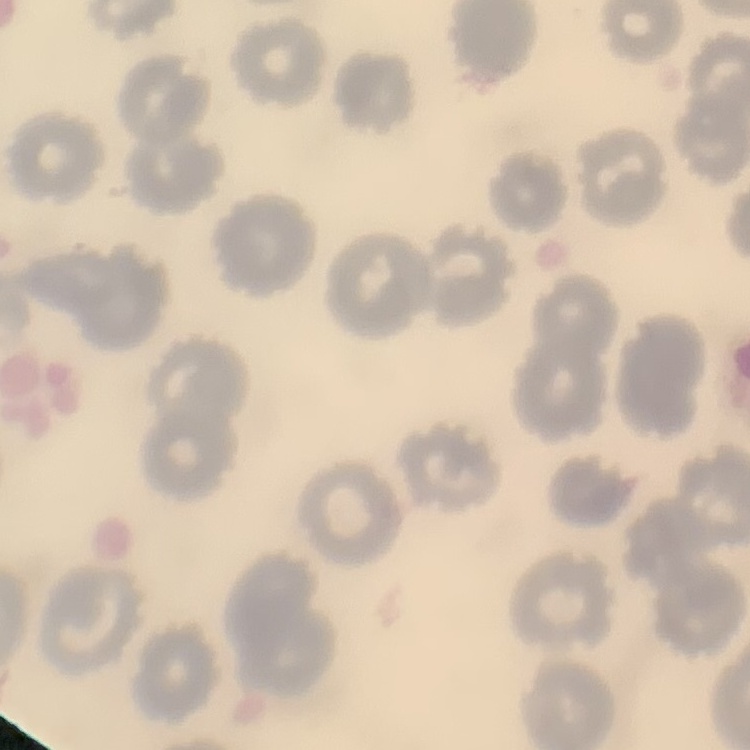
The red blood cells exhibit no rouleaux formation. Thin blood film. Stained with either Field's or Giemsa. Square crop of a larger photomicrograph.